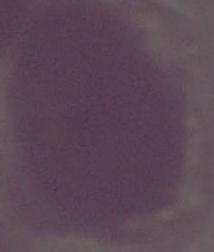

Summary:
  - Identification: red blood cell
  - Modality: micrograph
  - Magnification: 1000x